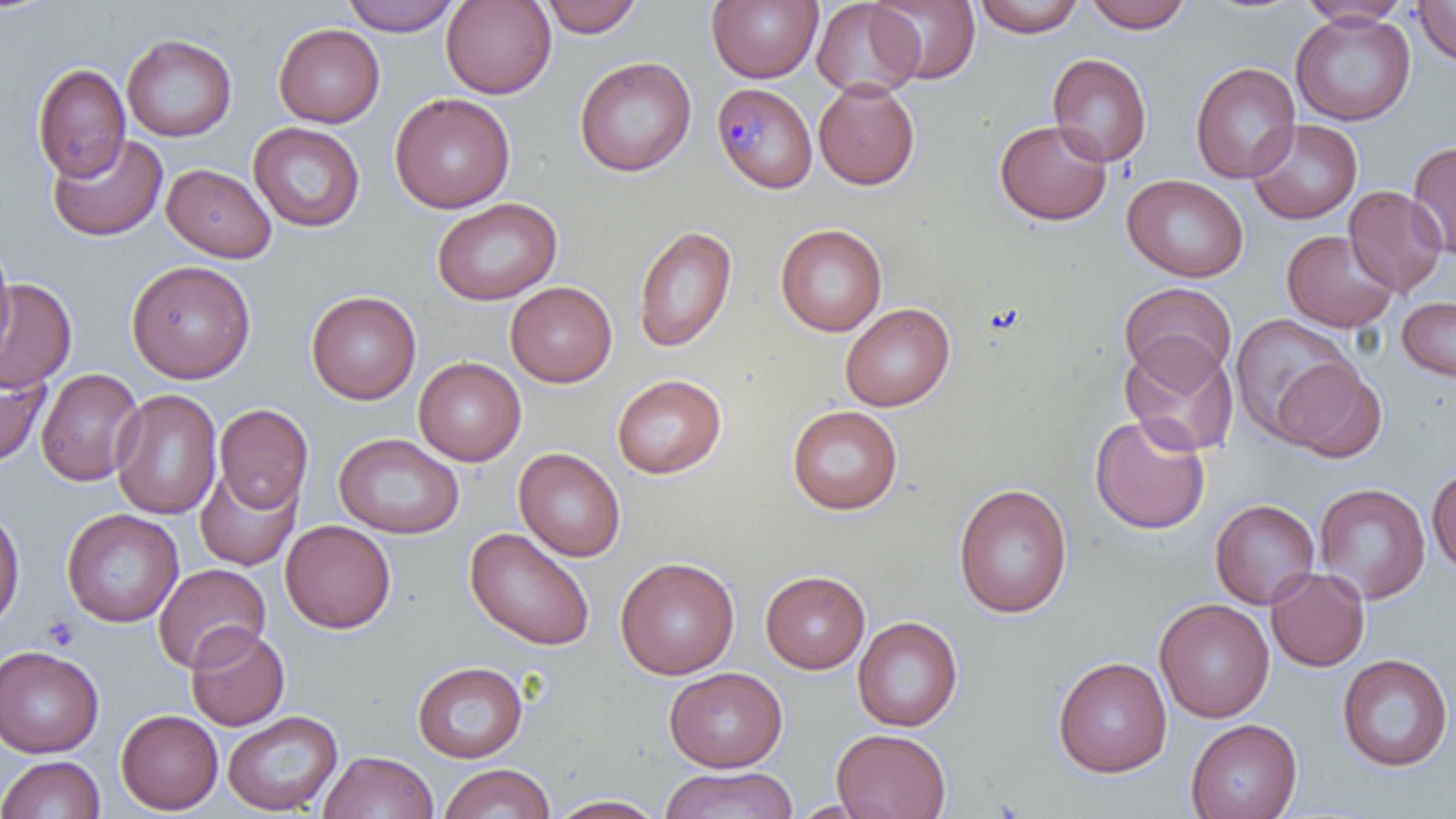
Approximate bounding boxes as (x1, y1, x2, y2) in pixels. Uninfected red blood cell locations: (339, 0, 462, 36), (441, 0, 556, 98), (540, 0, 645, 38), (707, 0, 822, 84), (811, 0, 922, 100), (868, 0, 981, 85), (972, 0, 1086, 38), (1082, 0, 1195, 33), (1412, 0, 1456, 66), (1297, 1, 1413, 26), (1291, 11, 1416, 126), (273, 23, 385, 128), (122, 33, 237, 142), (1046, 53, 1153, 167), (575, 56, 696, 177), (32, 62, 130, 183), (1189, 62, 1301, 183), (814, 79, 920, 190), (390, 92, 515, 213), (1246, 118, 1362, 224), (994, 119, 1112, 225), (248, 122, 365, 232), (47, 132, 167, 242), (1406, 140, 1456, 259), (162, 163, 276, 262), (1122, 174, 1248, 282), (1344, 185, 1448, 297), (431, 197, 562, 305), (632, 224, 738, 353), (775, 224, 887, 336), (1281, 230, 1399, 332), (0, 235, 15, 359), (126, 259, 256, 384), (0, 278, 77, 392), (505, 281, 617, 387), (1120, 281, 1236, 387), (305, 290, 421, 405), (1397, 296, 1456, 383), (840, 302, 955, 411), (1228, 313, 1358, 443), (1118, 338, 1238, 457), (413, 356, 526, 466), (1272, 357, 1387, 463), (0, 361, 51, 467), (35, 368, 144, 486), (611, 374, 726, 478), (110, 389, 222, 520), (214, 404, 313, 513), (787, 405, 903, 515), (1089, 413, 1210, 534), (333, 433, 464, 539), (513, 447, 625, 562), (194, 465, 302, 570), (1427, 465, 1456, 574), (1313, 482, 1430, 604), (952, 483, 1073, 619), (1210, 499, 1320, 609), (0, 504, 25, 632), (61, 508, 183, 627), (280, 520, 396, 633), (464, 527, 596, 651), (615, 556, 739, 680), (153, 563, 270, 672), (1266, 567, 1370, 672), (760, 570, 871, 673), (1154, 598, 1274, 722), (852, 616, 963, 732), (185, 624, 290, 731), (0, 645, 104, 757), (1337, 653, 1454, 773), (1053, 656, 1173, 778), (412, 661, 528, 763), (664, 667, 787, 772), (115, 709, 223, 814), (222, 711, 343, 815), (1185, 718, 1302, 819), (831, 728, 953, 819), (319, 751, 438, 819), (0, 755, 105, 819), (438, 763, 556, 819), (660, 766, 797, 819), (546, 794, 668, 818). Plasmodium malariae-infected red blood cell locations: (711, 81, 817, 193). Platelet locations: (43, 614, 80, 651). Slide-level diagnosis: Plasmodium malariae. One field of a larger specimen. Thin blood smear. Light microscopy. May-Grünwald-Giemsa stain. Captured at 1000x magnification. Image is 1456×819 pixels.